Give the position of every Plasmodium parasite.
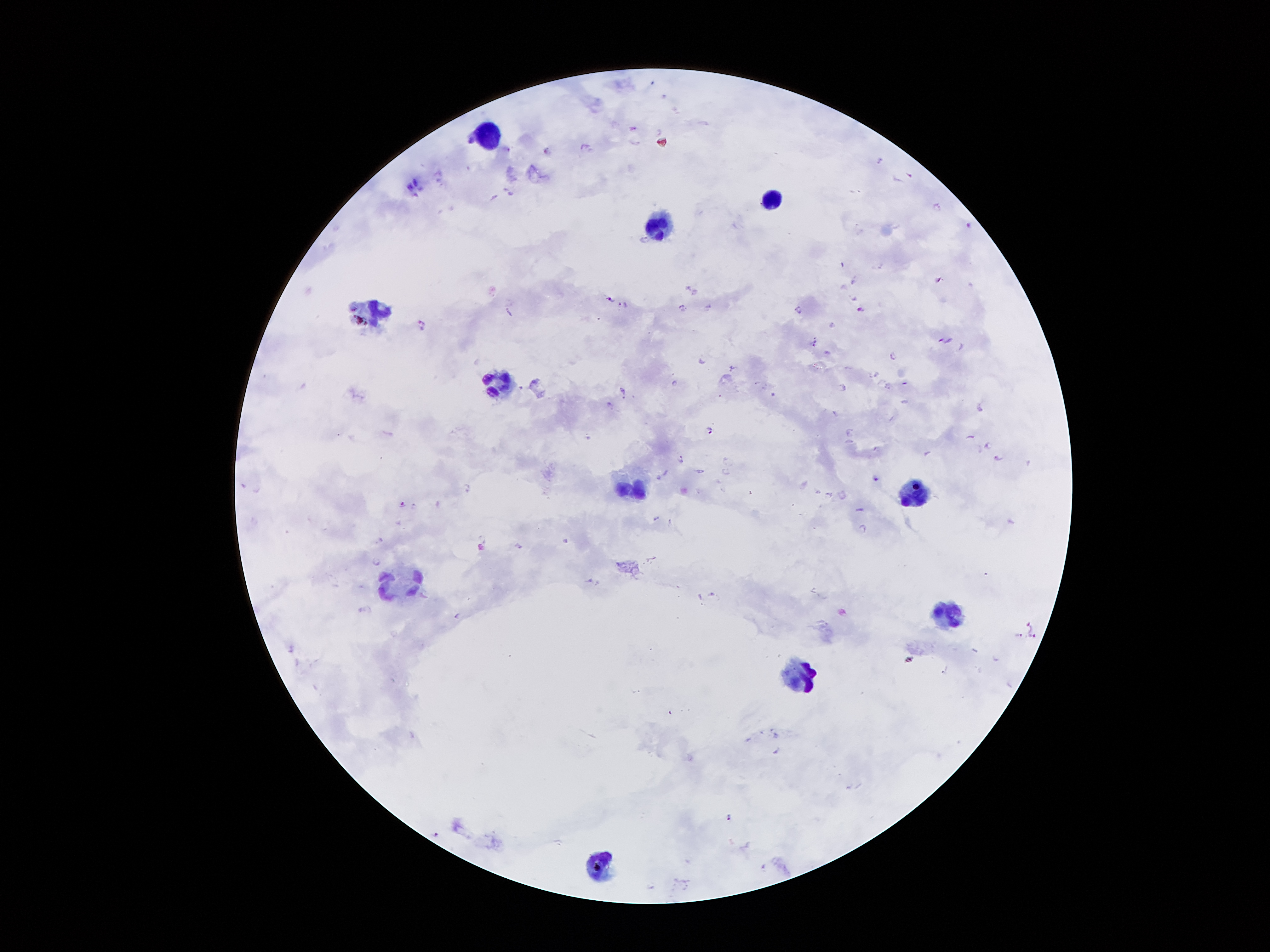
Approximate centers as {x, y} in pixels.
Plasmodium parasites: {634, 128}, {586, 144}, {545, 151}, {878, 160}, {910, 176}, {510, 190}, {936, 205}, {968, 224}, {643, 238}, {853, 280}, {939, 280}, {609, 298}, {623, 304}, {681, 305}, {708, 307}, {858, 308}, {798, 309}, {509, 311}, {421, 322}, {945, 339}, {814, 342}, {892, 356}, {702, 358}, {732, 367}, {903, 381}, {673, 382}, {843, 388}, {623, 390}, {608, 405}, {836, 413}, {709, 430}, {849, 431}, {971, 436}, {986, 445}, {874, 449}, {925, 452}, {994, 456}, {680, 458}, {728, 461}, {701, 470}, {724, 471}, {660, 475}, {876, 479}, {466, 485}, {817, 492}, {829, 494}, {843, 497}, {402, 503}, {859, 508}, {654, 517}, {863, 527}, {480, 537}, {378, 539}, {566, 540}, {517, 547}, {376, 559}, {590, 581}, {711, 591}, {360, 610}, {455, 616}, {1028, 623}, {1034, 634}, {1017, 635}, {729, 817}, {434, 835}, {761, 865}, {649, 886}.

Leukocyte locations: {488, 137}, {769, 202}, {662, 224}, {375, 311}, {500, 385}, {630, 490}, {915, 494}, {402, 581}, {948, 615}, {806, 675}, {601, 862}. 100x magnification. Giemsa stain. Patient malaria status: positive for Plasmodium falciparum. Image is 1270×952 pixels. Single field of view. Thick blood film. Smartphone photograph taken through the microscope eyepiece.